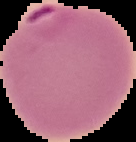
malaria status = parasitized
image size = 136×142 pixels
image type = cell region segmented out of the field of view; surrounding area masked to black
preparation = thin blood film